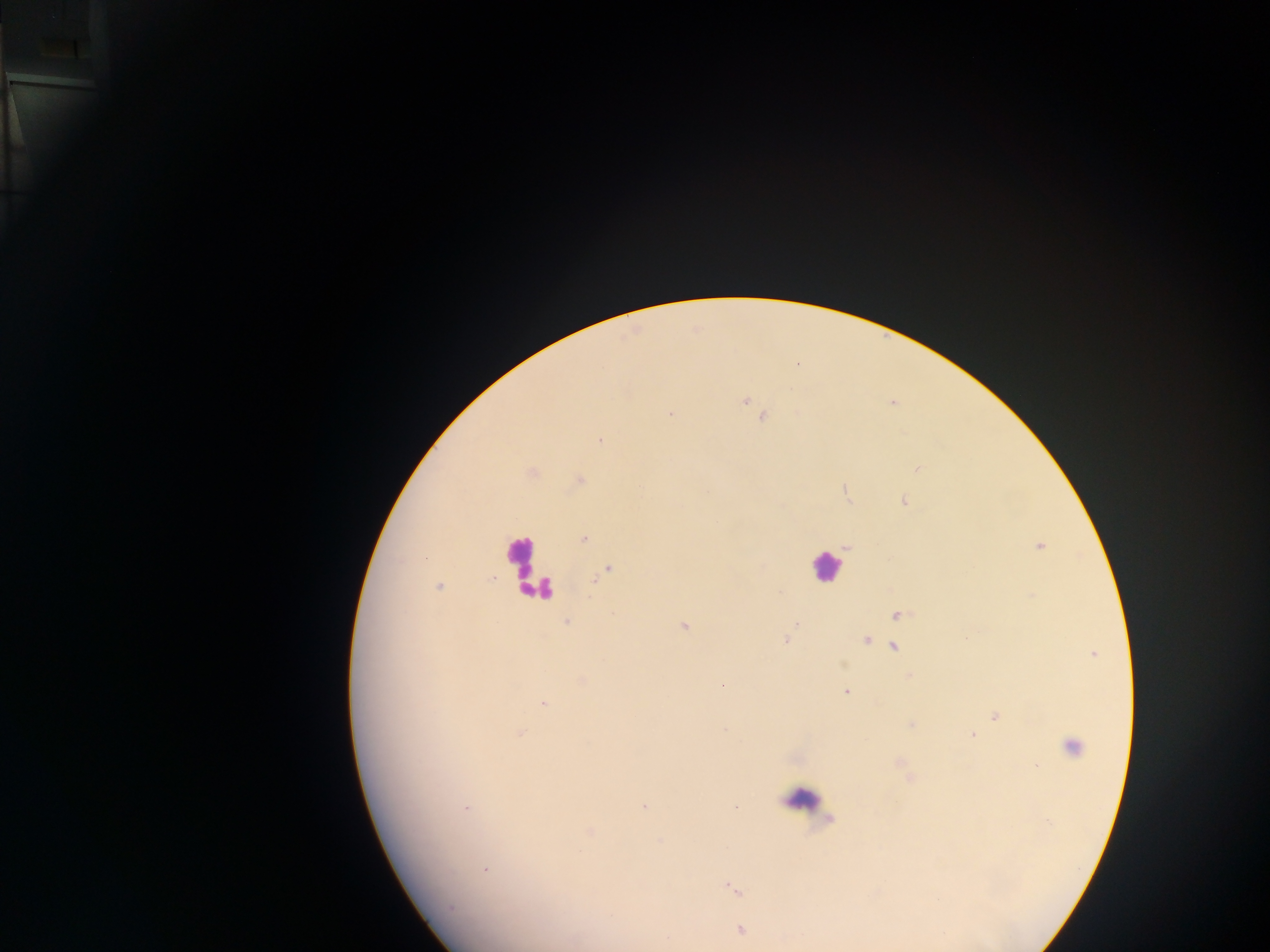

Approximate centers as x y in pixels. Leukocyte locations: 523 562; 826 566; 801 798. Malaria parasite locations: 745 400; 670 414; 762 417; 600 441; 917 468; 904 502; 584 539; 1039 546; 608 570; 439 586; 898 614; 566 622; 795 625; 683 626; 786 639; 866 640; 893 647; 909 675; 722 684; 846 691; 543 704; 996 715; 521 733; 972 735; 1071 747; 644 806; 467 809; 590 832; 485 871; 732 889; 450 907; 741 929. Image is 1270×952 pixels. Thick blood film. Sample from Ghana. One field of view. Mobile-phone photograph taken through the microscope.